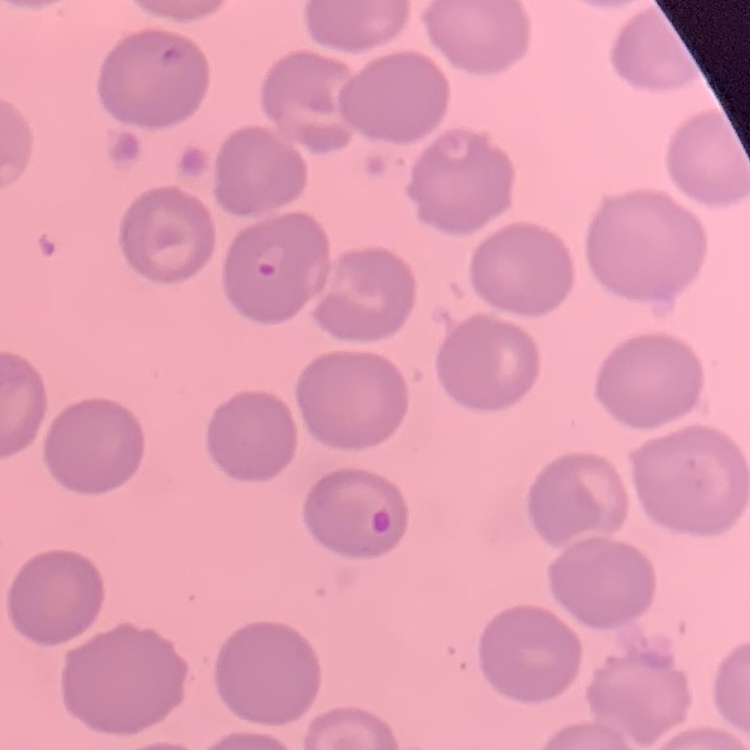
Summary:
  - Erythrocyte morphology: no rouleaux formation
  - Preparation: thin peripheral smear
  - Image type: one tile cut from a larger photomicrograph
  - Stain: Field's or Giemsa